Describe the morphology of the red blood cells.
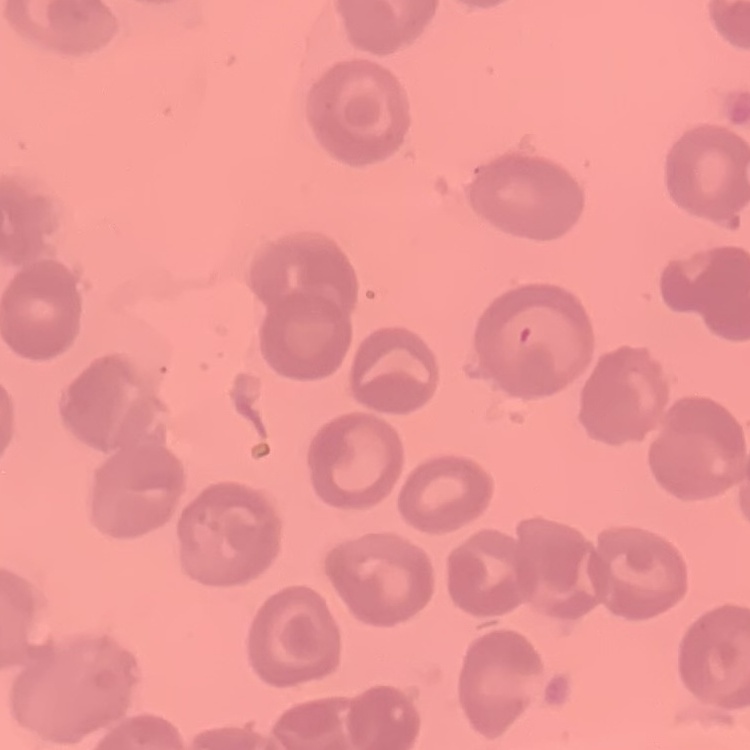

They show no rouleaux formation.

preparation = thin blood film
stain = Field's or Giemsa
image type = one tile cut from a larger photomicrograph